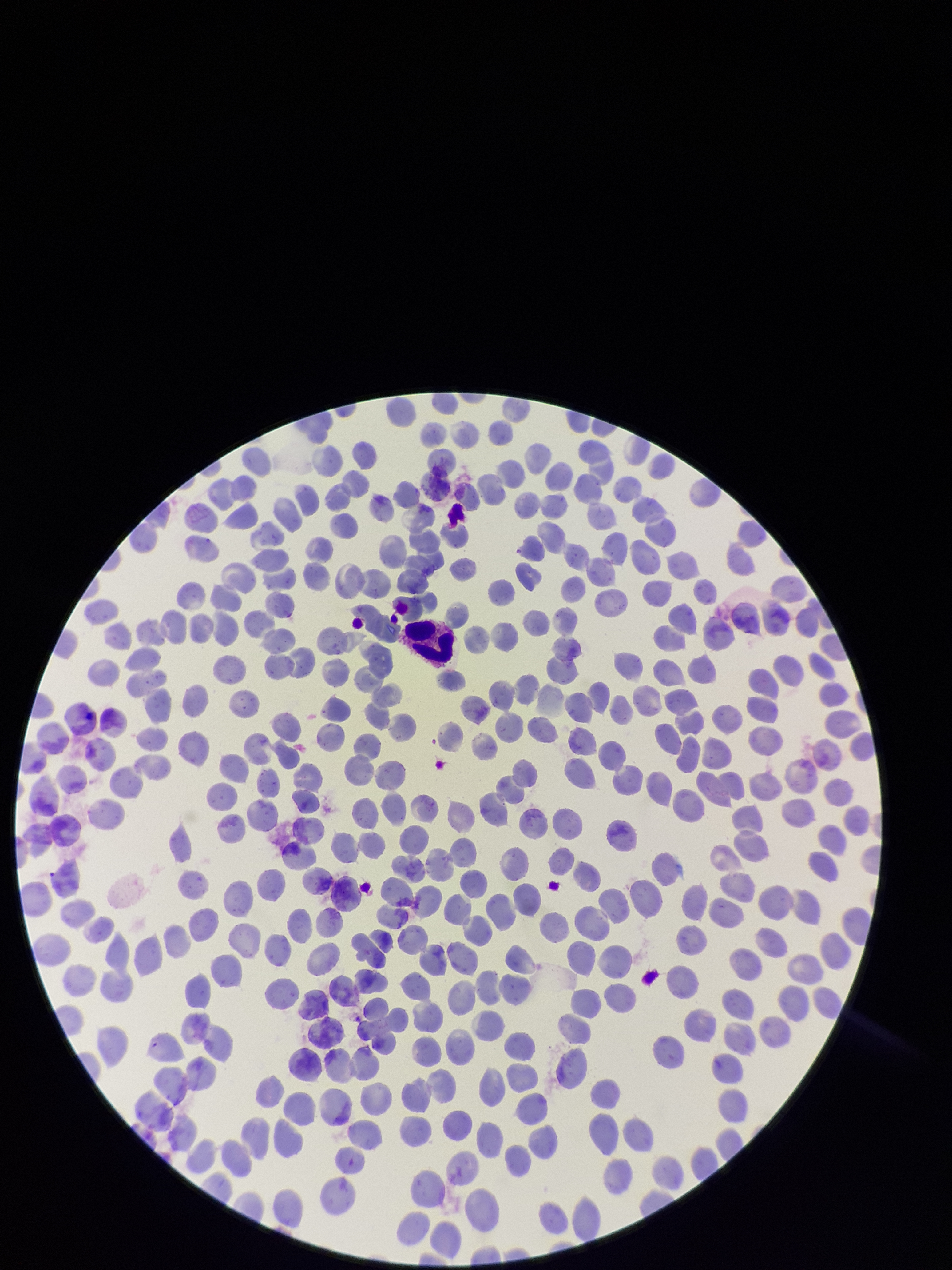
Summary:
  - Image size: 952×1270 pixels
  - Patient malaria status: negative
  - Parasitized red blood cell count: 0
  - Parasitized red blood cells: none seen
  - Preparation: thin blood smear
  - Field of view: single
  - Red blood cell count: 353
  - Stain: Giemsa
  - Capture: smartphone photograph through the microscope eyepiece